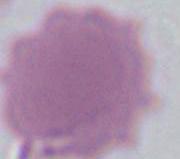
Captured at 1000x magnification. Micrograph. An erythrocyte is seen.